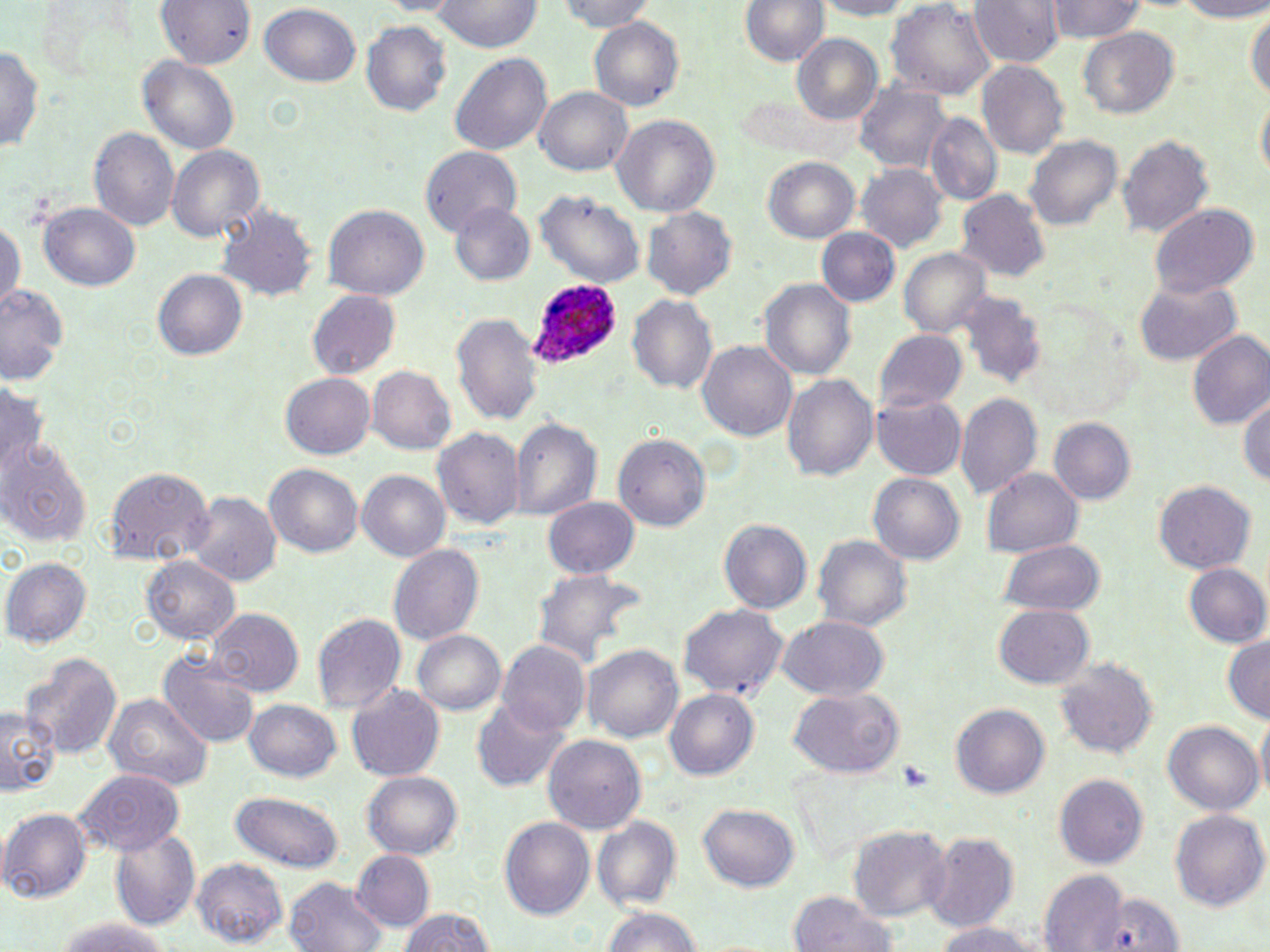

slide-level diagnosis = Plasmodium ovale
image size = 1270×952 pixels
uninfected red blood cell locations = approximate bounding boxes as (x1,y1)-(x2,y2) corner pairs in pixels: (154,0)-(251,72), (433,0)-(543,53), (560,0)-(659,30), (740,0)-(830,72), (809,0)-(917,18), (887,0)-(997,101), (967,0)-(1060,69), (1043,0)-(1149,46), (1159,0)-(1270,20), (260,2)-(362,87), (1247,4)-(1269,112), (589,16)-(686,110), (360,19)-(452,120), (1078,26)-(1179,119), (789,33)-(883,126), (0,35)-(44,157), (449,52)-(554,160), (137,54)-(242,159), (978,60)-(1069,159), (854,85)-(951,174), (534,86)-(634,177), (925,112)-(1002,204), (610,113)-(719,219), (88,128)-(179,233), (1117,132)-(1215,243), (1023,133)-(1122,232), (168,145)-(264,244), (421,145)-(523,237), (762,156)-(862,245), (856,164)-(948,253), (958,191)-(1052,282), (535,193)-(645,287), (37,201)-(138,291), (452,202)-(535,287), (324,205)-(428,300), (642,205)-(737,299), (1150,205)-(1258,301), (213,206)-(319,302), (0,212)-(24,317), (818,228)-(901,308), (901,248)-(991,341), (152,268)-(247,361), (759,276)-(856,383), (1133,279)-(1241,365), (0,283)-(71,380), (306,292)-(400,381), (958,293)-(1044,386), (628,294)-(719,397), (452,314)-(543,425), (875,330)-(966,415), (1187,330)-(1270,431), (697,340)-(796,442), (367,365)-(457,455), (781,372)-(878,482), (280,374)-(374,460), (1240,386)-(1270,493), (871,391)-(968,479), (957,392)-(1042,499), (511,416)-(600,523), (1048,418)-(1133,505), (433,426)-(521,533), (614,432)-(712,533), (2,436)-(89,545), (264,464)-(363,559), (104,467)-(214,566), (981,469)-(1084,557), (357,471)-(452,564), (868,473)-(965,566), (1154,479)-(1256,573), (186,489)-(279,589), (544,495)-(641,580), (719,519)-(811,616), (814,535)-(912,636), (1000,540)-(1106,618), (388,545)-(483,647), (141,554)-(240,646), (5,557)-(91,647), (1183,562)-(1270,652), (533,572)-(643,669), (675,603)-(788,704), (993,605)-(1093,690), (212,610)-(301,695), (312,613)-(406,716), (776,615)-(891,701), (412,630)-(507,717), (1220,634)-(1270,724), (499,642)-(590,740), (582,642)-(684,745), (160,650)-(261,746), (22,651)-(120,763), (1056,657)-(1158,760), (347,686)-(446,782), (664,688)-(760,782), (788,688)-(905,778), (103,694)-(210,793), (471,694)-(569,793), (245,700)-(343,784), (951,702)-(1050,800), (0,705)-(58,796), (1165,721)-(1262,818), (543,734)-(646,836), (75,769)-(184,854), (362,770)-(464,859), (1055,775)-(1148,871), (229,790)-(345,873), (698,802)-(799,893), (2,807)-(92,901), (1169,808)-(1268,913), (499,815)-(596,923), (593,816)-(683,914), (848,825)-(950,922), (109,830)-(201,930), (922,832)-(1020,928), (350,851)-(433,933), (194,857)-(288,945), (1039,872)-(1126,951), (285,876)-(388,952), (785,890)-(899,952), (394,907)-(502,952), (604,907)-(701,952), (46,918)-(181,952), (932,921)-(1045,952)
stain = May-Grünwald-Giemsa
magnification = 1000x
Plasmodium ovale-infected red blood cell locations = approximate bounding boxes as (x1,y1)-(x2,y2) corner pairs in pixels: (528,282)-(622,370)
field of view = single
preparation = thin blood film
modality = light microscopy